Classify this cell by malaria status.
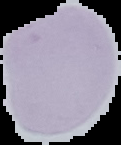
It is uninfected.

preparation = thin blood smear
image size = 121×145 pixels
image type = segmented cell region with the area outside set to black